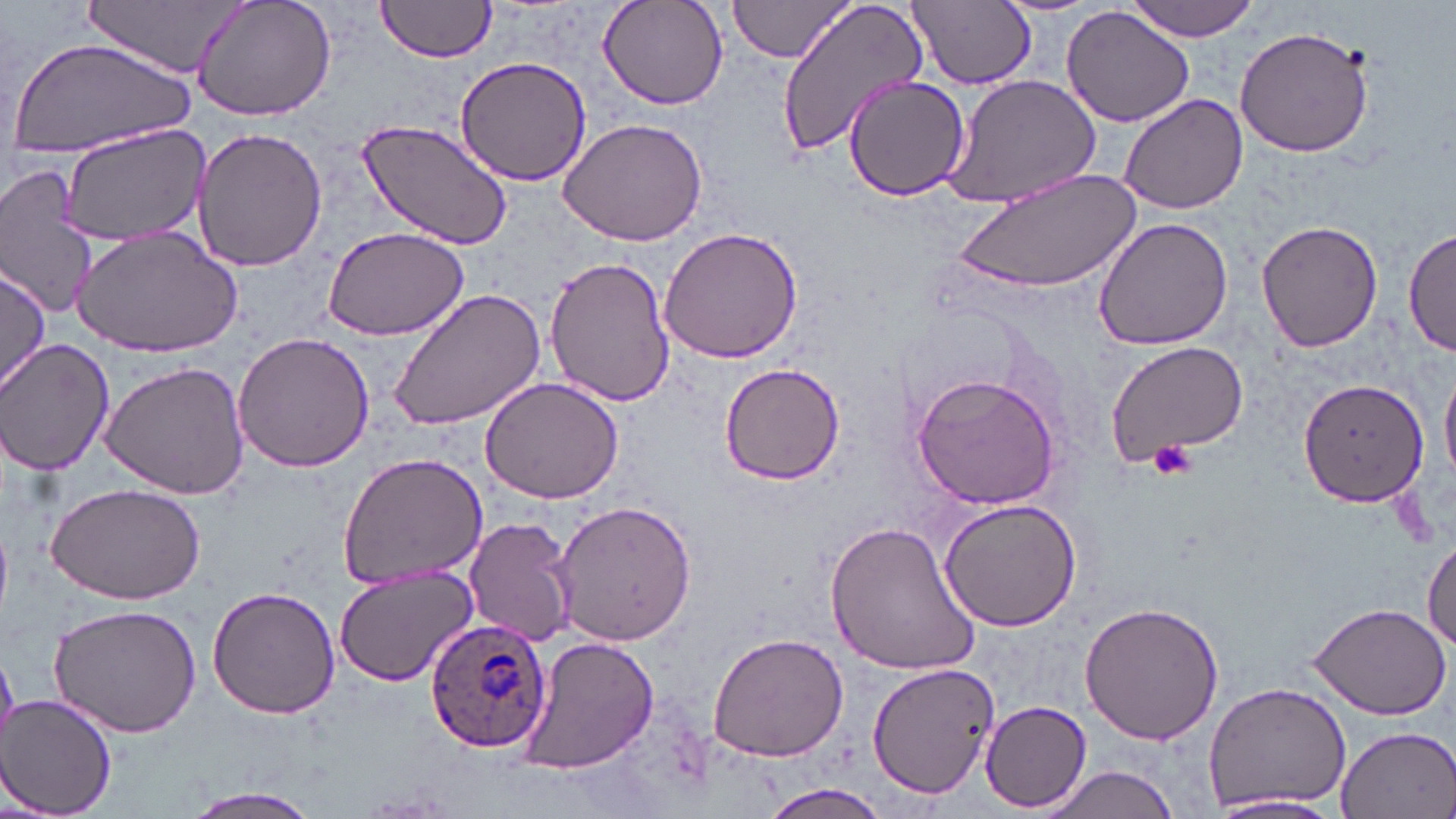

Summary:
  - Coordinate format: approximate bounding boxes as (x1,y1)-(x2,y2) corner pairs in pixels
  - Uninfected red blood cell locations: (88,0)-(252,79), (189,0)-(338,123), (373,0)-(493,65), (725,0)-(857,67), (776,0)-(929,157), (907,0)-(1036,89), (994,0)-(1098,18), (597,1)-(728,109), (1122,1)-(1266,40), (1061,8)-(1196,128), (1234,25)-(1376,159), (7,37)-(195,158), (454,56)-(592,187), (942,74)-(1101,211), (843,76)-(971,202), (1119,94)-(1247,214), (560,116)-(707,248), (358,118)-(512,249), (55,125)-(209,244), (192,128)-(329,271), (0,160)-(103,319), (955,168)-(1144,298), (1092,216)-(1234,351), (1255,221)-(1385,353), (75,223)-(243,357), (656,225)-(807,365), (322,226)-(470,342), (1405,226)-(1456,361), (544,256)-(676,409), (0,263)-(50,398), (387,286)-(547,434), (231,330)-(374,475), (1,340)-(116,475), (1103,341)-(1248,467), (100,362)-(251,501), (720,362)-(845,486), (1440,366)-(1456,486), (911,369)-(1065,511), (479,374)-(626,505), (1298,376)-(1430,508), (336,452)-(489,590), (45,482)-(206,605), (938,496)-(1083,632), (553,500)-(697,648), (464,515)-(578,648), (825,520)-(984,677), (1423,538)-(1456,657), (332,563)-(480,686), (208,584)-(341,720), (1079,600)-(1226,747), (1304,600)-(1454,719), (46,602)-(202,738), (705,632)-(849,762), (519,634)-(662,773), (866,662)-(998,800), (1202,681)-(1352,812), (2,695)-(118,817), (981,701)-(1092,813), (1333,725)-(1456,819), (1034,764)-(1184,819), (757,782)-(890,819), (182,785)-(326,818), (1210,794)-(1347,817)
  - Platelet locations: (1147,439)-(1197,480)
  - Plasmodium ovale-infected red blood cell locations: (426,616)-(552,754)
  - Slide-level diagnosis: Plasmodium ovale
  - Preparation: thin blood smear
  - Modality: light microscopy
  - Field of view: one of a larger specimen
  - Image size: 1456×819 pixels
  - Stain: May-Grünwald-Giemsa
  - Magnification: 1000x